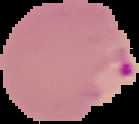

image type = segmented cell region with the area outside set to black
malaria status = parasitized
image size = 139×124 pixels
preparation = thin blood smear